State which parasite is depicted.
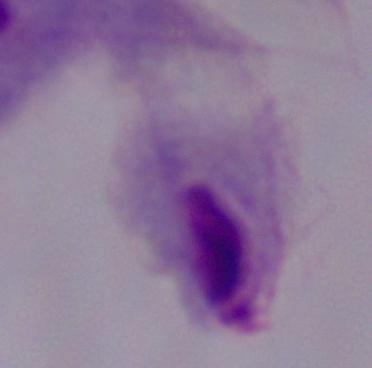
This is a trichomonad.

magnification = 1000x
modality = photomicrograph